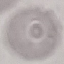

result = no malaria parasites detected
stain = Giemsa
capture = smartphone through the microscope eyepiece
preparation = thin blood smear
image type = cell patch, automatically extracted from a larger field of view and resized to 64 × 64 pixels